Describe the morphology of the red blood cells.
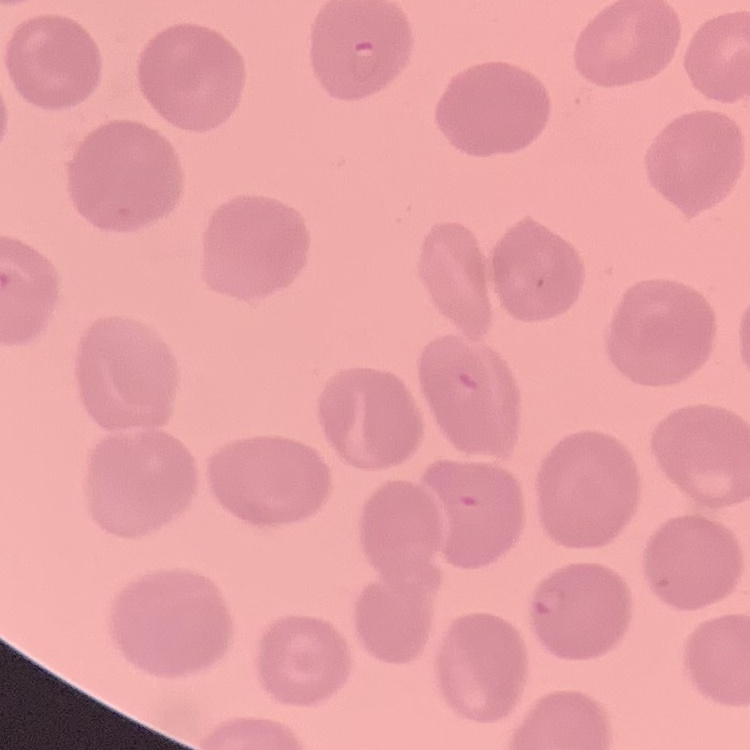

They show no rouleaux formation.

Summary:
  - Stain: Field's or Giemsa
  - Image type: square crop of a larger photomicrograph
  - Preparation: thin peripheral smear